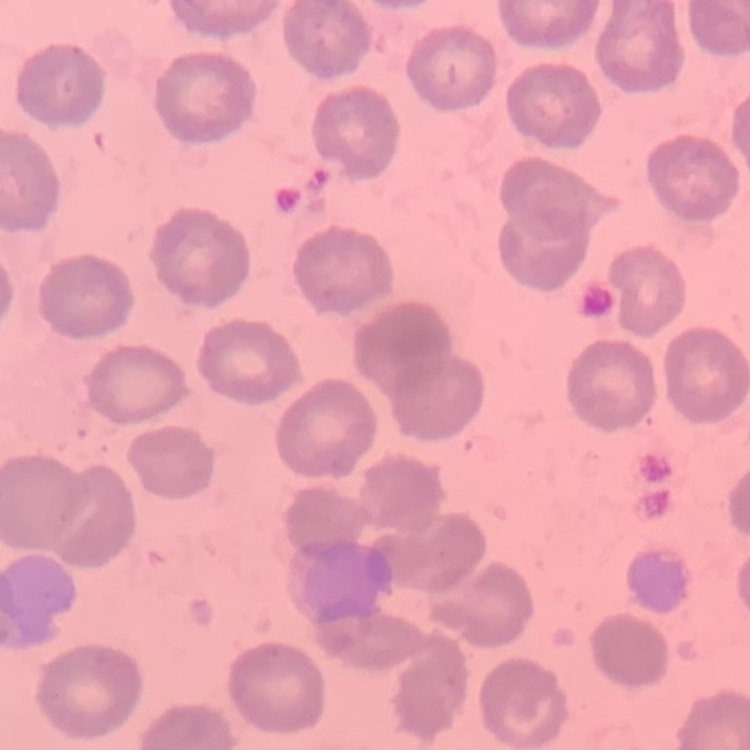

erythrocyte morphology = no rouleaux formation
preparation = thin blood smear
image type = one tile cut from a larger photomicrograph
stain = Field's or Giemsa